Give the position of every Plasmodium parasite.
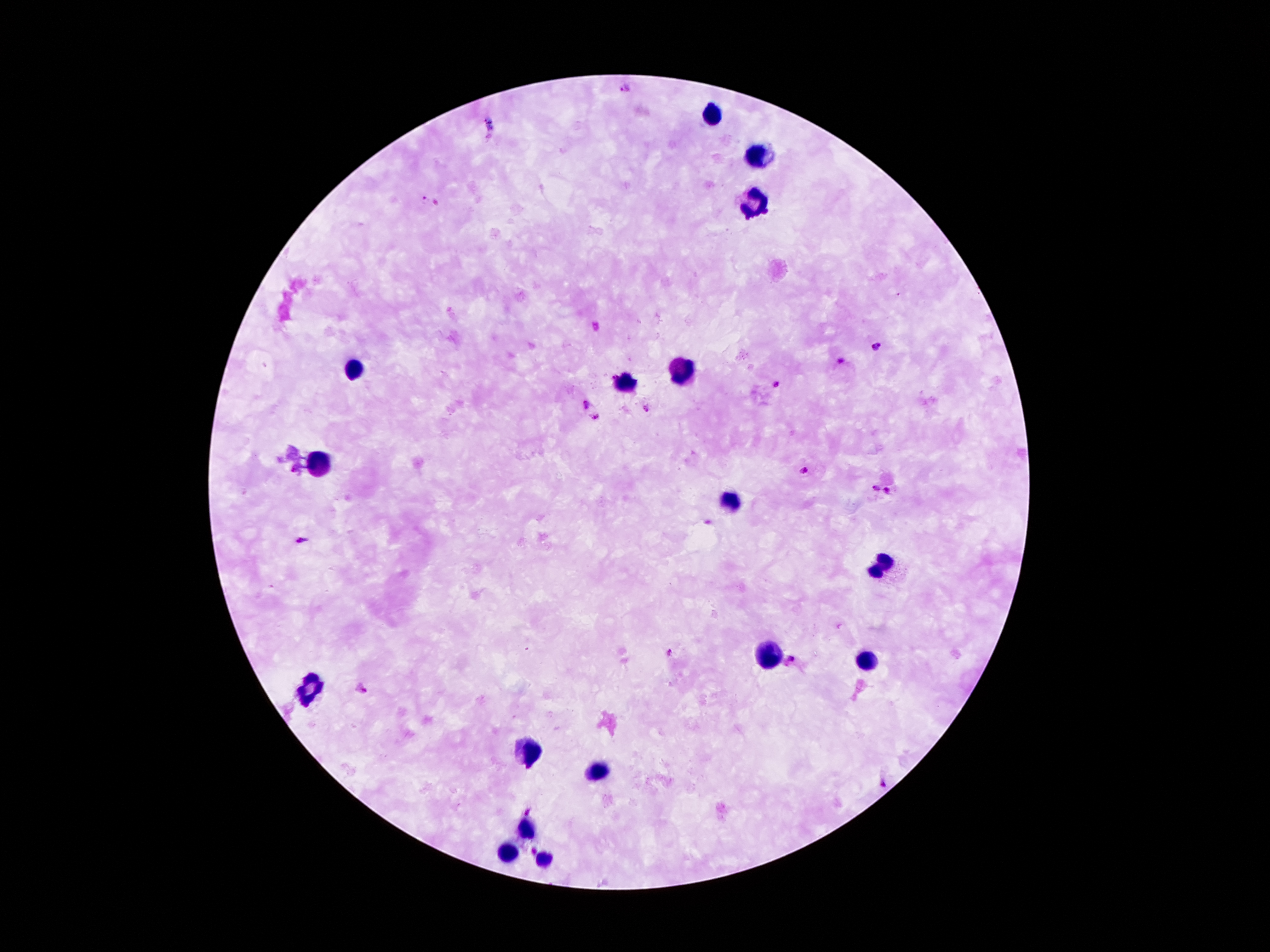
Approximate centers as [x, y] in pixels.
Plasmodium parasites: [626, 87], [423, 198], [875, 347], [840, 360], [777, 385], [585, 405], [646, 410], [595, 417], [803, 470], [876, 487], [888, 492], [302, 540], [668, 652], [791, 658], [360, 687], [882, 785], [528, 811], [534, 851].

Leukocyte locations: [711, 114], [754, 162], [751, 200], [351, 366], [684, 370], [625, 383], [318, 462], [730, 497], [881, 562], [771, 654], [866, 662], [310, 690], [531, 750], [595, 772], [526, 829], [507, 851], [543, 861]. Thick blood film. Single field of view. 100x magnification. Giemsa-stained preparation. Image is 1270×952 pixels. Patient malaria status: positive for Plasmodium falciparum. Smartphone photograph taken through the microscope eyepiece.